Give the position of every Plasmodium parasite and every leukocyte.
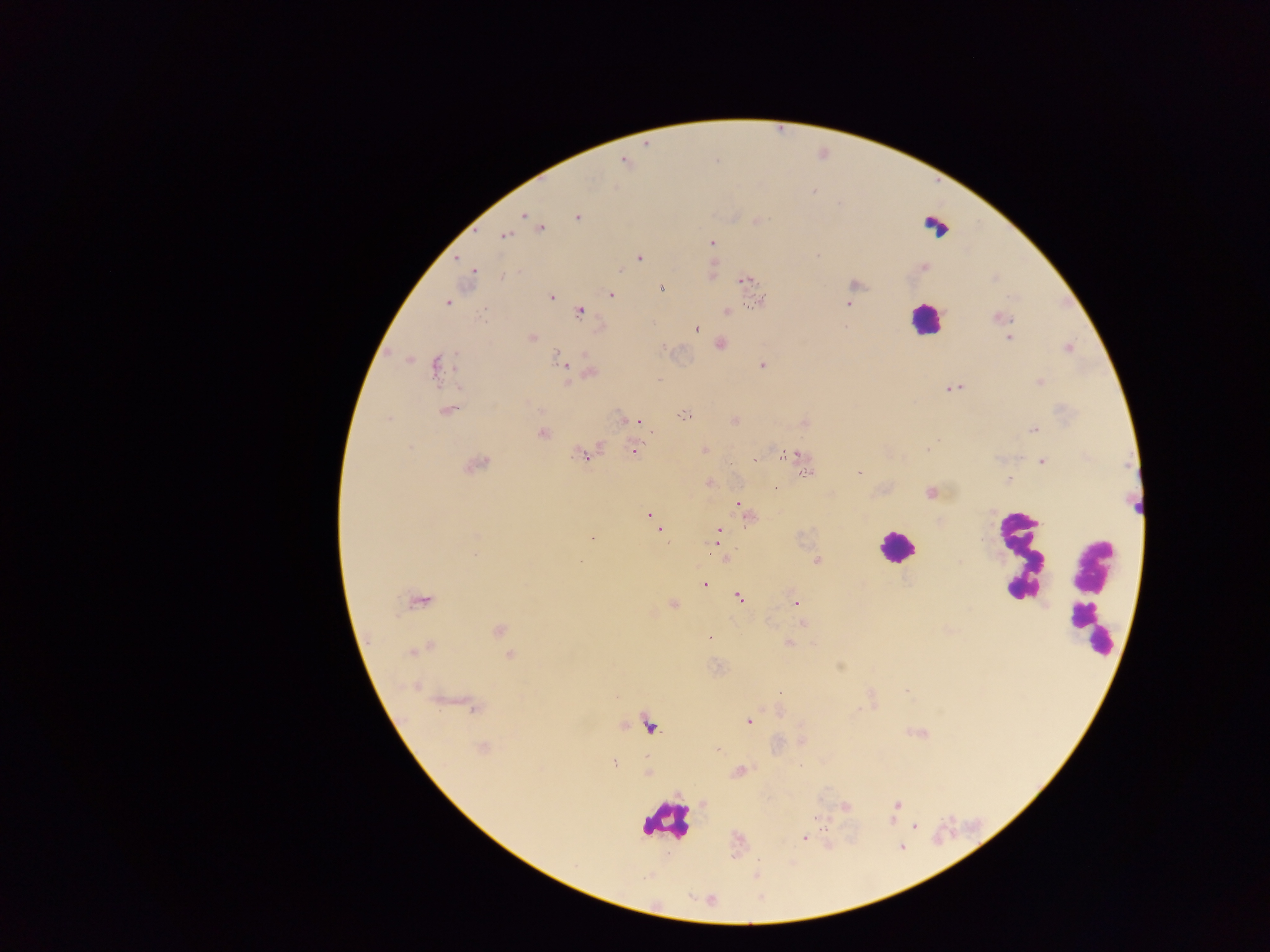

Approximate centers as x y in pixels.
Plasmodium parasites: 623 160; 813 191; 524 215; 577 217; 541 228; 504 236; 712 242; 458 258; 639 258; 472 271; 745 280; 661 289; 611 295; 551 296; 760 301; 446 303; 848 304; 727 311; 579 312; 998 318; 696 328; 531 337; 1009 339; 720 344; 1068 348; 558 358; 762 365; 435 366; 591 372; 1040 381; 953 388; 446 412; 683 415; 388 418; 623 419; 634 420; 734 420; 1034 429; 542 433; 409 448; 927 448; 703 450; 634 451; 581 455; 783 455; 795 455; 1042 462; 476 465; 859 473; 806 475; 1009 479; 709 483; 931 493; 739 505; 747 516; 650 517; 655 523; 660 531; 718 534; 592 539; 718 542; 816 560; 705 584; 739 598; 418 601; 795 603; 673 604; 802 623; 499 630; 710 638; 789 643; 416 651; 510 654; 906 690; 779 692; 474 707; 748 722; 649 726; 483 747; 614 763; 739 771; 897 805; 846 807; 916 827; 804 839.
Leukocytes: 937 225; 924 319; 1138 491; 893 546; 1018 553; 1091 593; 665 821.

Image is 1270×952 pixels. Thick blood smear. Collected in Ghana. Single field of view. Photographed through a microscope with a mobile-phone camera.